Assess this cell for malaria.
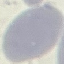
It is uninfected.

{
  "capture": "smartphone through the microscope eyepiece",
  "stain": "Giemsa",
  "image_type": "cell patch, automatically extracted from a larger field of view and resized to 64 × 64 pixels",
  "preparation": "thin smear"
}